Classify this cell by malaria status.
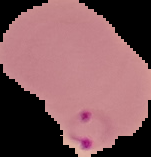
It is parasitized.

{
  "image_size": "151×157 pixels",
  "image_type": "segmented cell region with the area outside set to black",
  "preparation": "thin blood film"
}